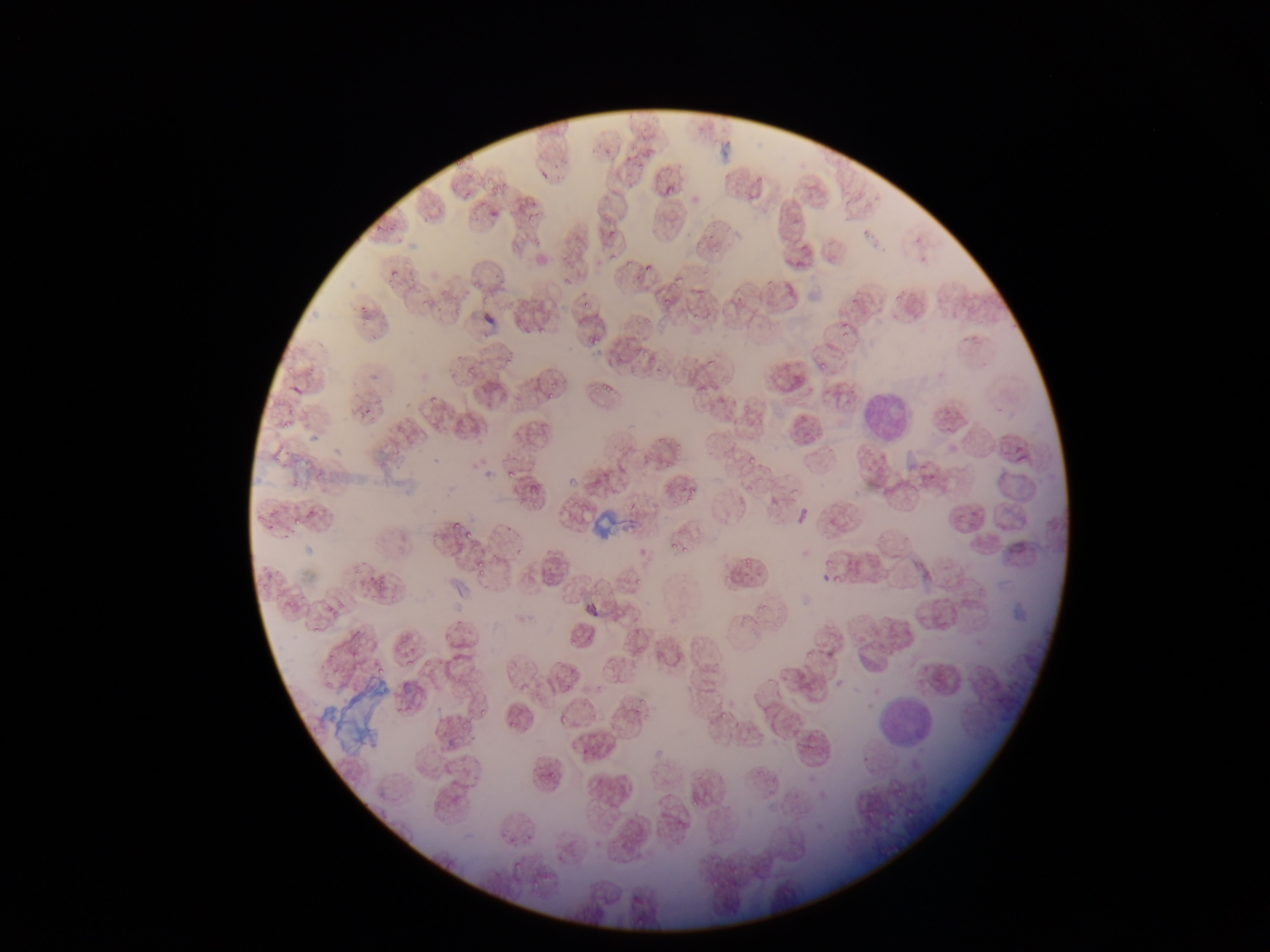
Approximate bounding boxes as left top right bottom in pixels. Malaria parasite locations: 662 180 677 195; 489 208 502 222; 641 246 659 270; 386 258 406 284; 658 293 676 315; 581 297 592 308; 425 298 436 311; 451 299 464 316; 841 327 853 340; 585 328 603 346; 498 351 519 370; 464 361 476 374; 545 379 565 389; 590 382 601 399; 605 384 616 394; 544 390 554 397; 423 394 438 406; 281 412 297 434; 393 436 407 453; 663 451 679 475; 499 464 520 479; 670 492 687 509; 305 503 321 520; 260 504 279 518; 448 514 461 531; 291 521 300 530; 460 528 472 541; 666 536 679 554; 681 540 689 556; 472 557 482 567; 821 557 834 568; 472 566 486 577; 829 568 842 590; 260 574 273 598; 368 574 387 592; 284 599 299 611; 304 618 323 640; 345 626 364 656; 399 633 414 655; 327 647 347 672; 421 659 431 677; 368 665 394 680; 478 702 487 717; 717 702 739 721; 558 707 571 726; 502 712 517 731; 641 714 658 725; 612 730 616 740; 676 782 694 816; 689 786 714 814; 510 857 524 873; 527 876 542 889. Leukocyte locations: 756 351 814 410; 854 382 918 448; 781 406 827 456; 869 689 942 755. Thin blood film. Sample from Ghana. One field of view. Mobile-phone photograph taken through the microscope. Image is 1270×952 pixels.